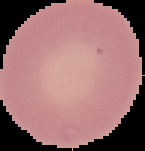
Summary:
  - Result: no Plasmodium parasites detected
  - Preparation: thin blood smear
  - Image type: segmented cell region with the area outside set to black
  - Image size: 145×151 pixels